Assess this cell for malaria.
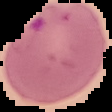
Parasitized.

Summary:
  - Image size: 112×112 pixels
  - Preparation: thin blood film
  - Image type: segmented cell region on a black background